Comment on the morphology of the red blood cells.
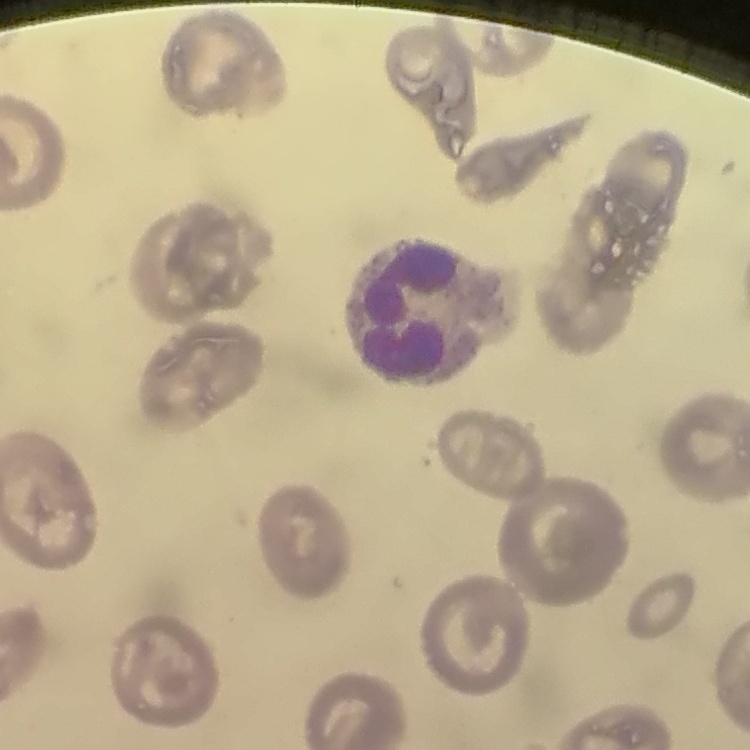
They show no rouleaux formation.

Stained with either Field's or Giemsa. Square crop of a larger photomicrograph. Thin peripheral smear.